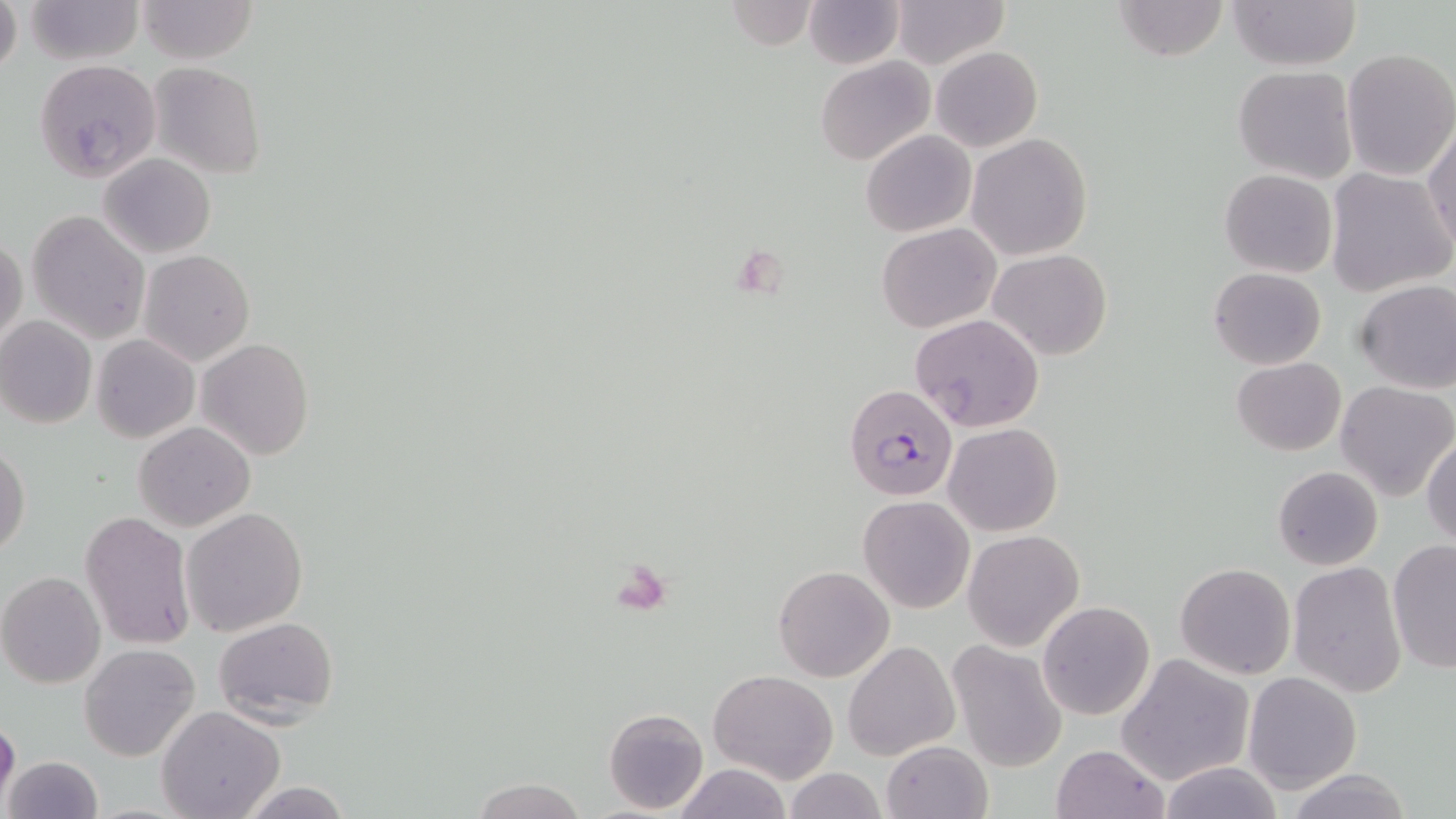

Summary:
  - Coordinate format: approximate bounding boxes as (x1,y1)-(x2,y2) corner pairs in pixels
  - Plasmodium falciparum-infected red blood cell locations: (844,383)-(959,505)
  - Uninfected red blood cell locations: (0,0)-(22,80), (23,0)-(145,66), (136,0)-(258,65), (803,0)-(905,70), (1112,0)-(1229,61), (1224,0)-(1361,70), (723,1)-(816,50), (889,1)-(1010,69), (932,46)-(1042,151), (1340,47)-(1456,182), (33,58)-(161,181), (816,58)-(934,166), (148,62)-(265,179), (1232,66)-(1358,184), (1424,127)-(1456,254), (862,130)-(975,237), (966,133)-(1093,260), (98,153)-(216,258), (1324,167)-(1453,297), (1219,169)-(1337,278), (26,209)-(149,344), (877,223)-(1000,332), (0,237)-(27,351), (988,248)-(1113,360), (138,249)-(254,365), (1208,266)-(1327,370), (1353,280)-(1456,393), (908,313)-(1044,433), (0,316)-(97,429), (90,334)-(198,443), (199,338)-(314,461), (1231,358)-(1346,455), (1335,380)-(1455,500), (133,421)-(254,531), (943,422)-(1063,536), (1422,432)-(1456,550), (1,443)-(29,559), (1272,467)-(1383,569), (859,494)-(976,613), (181,506)-(309,637), (81,510)-(195,649), (963,528)-(1085,651), (1388,538)-(1456,675), (1291,560)-(1405,697), (1174,563)-(1295,680), (772,565)-(894,683), (0,572)-(105,689), (1037,601)-(1156,722), (214,616)-(340,726), (946,639)-(1069,770), (844,640)-(961,760), (79,643)-(201,762), (1118,655)-(1253,786), (709,668)-(837,782), (1243,670)-(1362,794), (157,705)-(286,819), (604,707)-(709,814), (0,713)-(20,809), (881,740)-(992,818), (1052,744)-(1168,819), (3,754)-(103,819), (1156,762)-(1285,819), (673,763)-(792,818), (785,766)-(886,819), (470,777)-(588,819), (237,780)-(356,818)
  - Slide-level diagnosis: Plasmodium falciparum
  - Preparation: thin blood film
  - Field of view: single
  - Image size: 1456×819 pixels
  - Stain: May-Grünwald-Giemsa
  - Magnification: 1000x
  - Modality: light microscopy